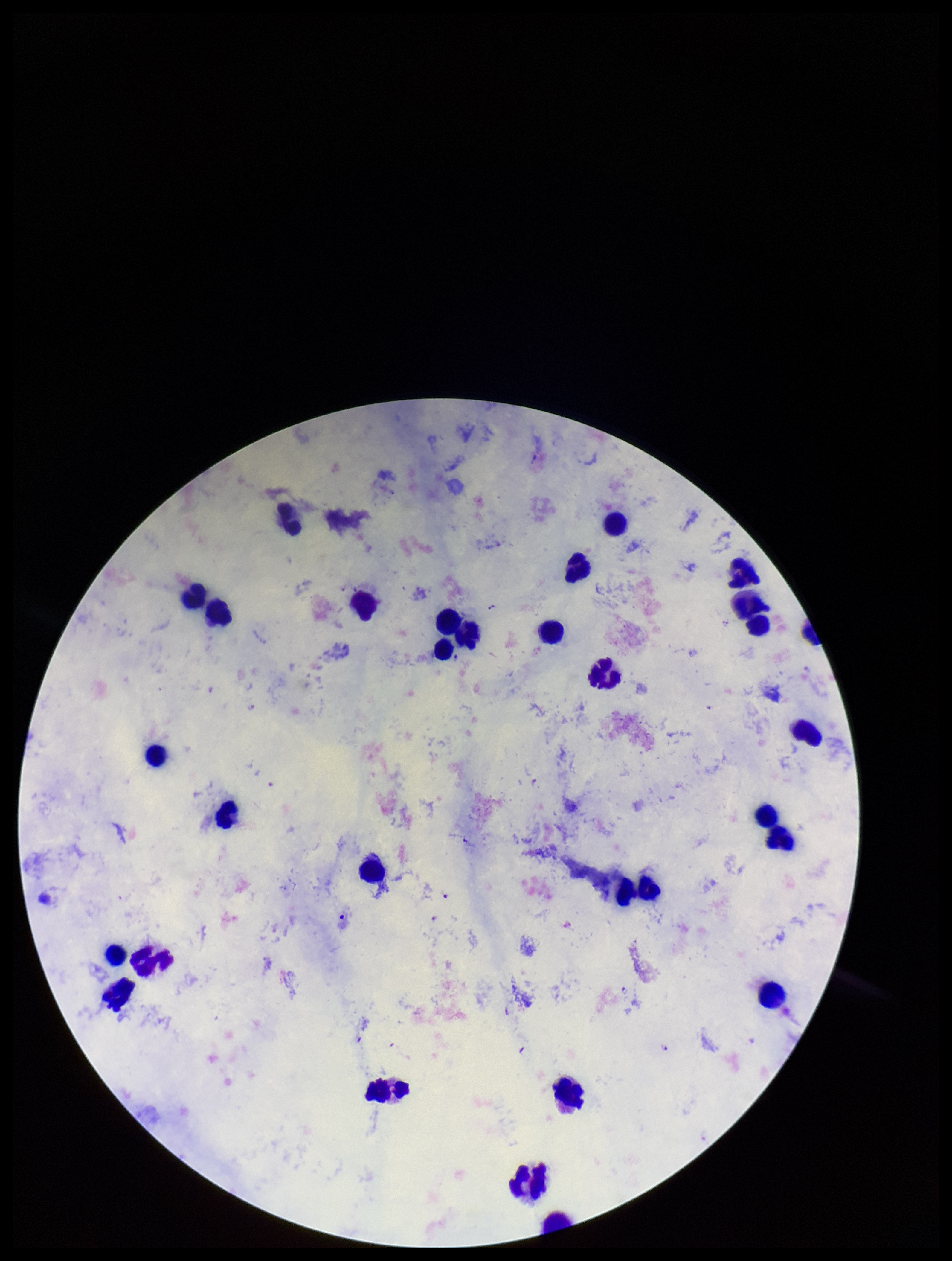

Plasmodium parasites: identified. Patient malaria status: positive. Image is 952×1261 pixels. Giemsa stain. Species reported for this patient: Plasmodium falciparum. Photographed through the microscope eyepiece with a smartphone camera. Leukocyte count: 32. Parasite count: 5. Single field of view. Preparation: thick blood smear.